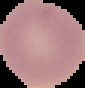
image_size: 85×88 pixels
image_type: segmented cell region on a black background
preparation: thin blood film
malaria_status: uninfected